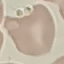

Summary:
  - Result: negative for malaria parasites
  - Capture: smartphone camera at the microscope eyepiece
  - Stain: Giemsa
  - Image type: automatically extracted cell patch, resized to 64 × 64 pixels
  - Preparation: thin blood film